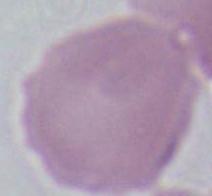

Captured at 1000x magnification. An erythrocyte is seen. Micrograph.